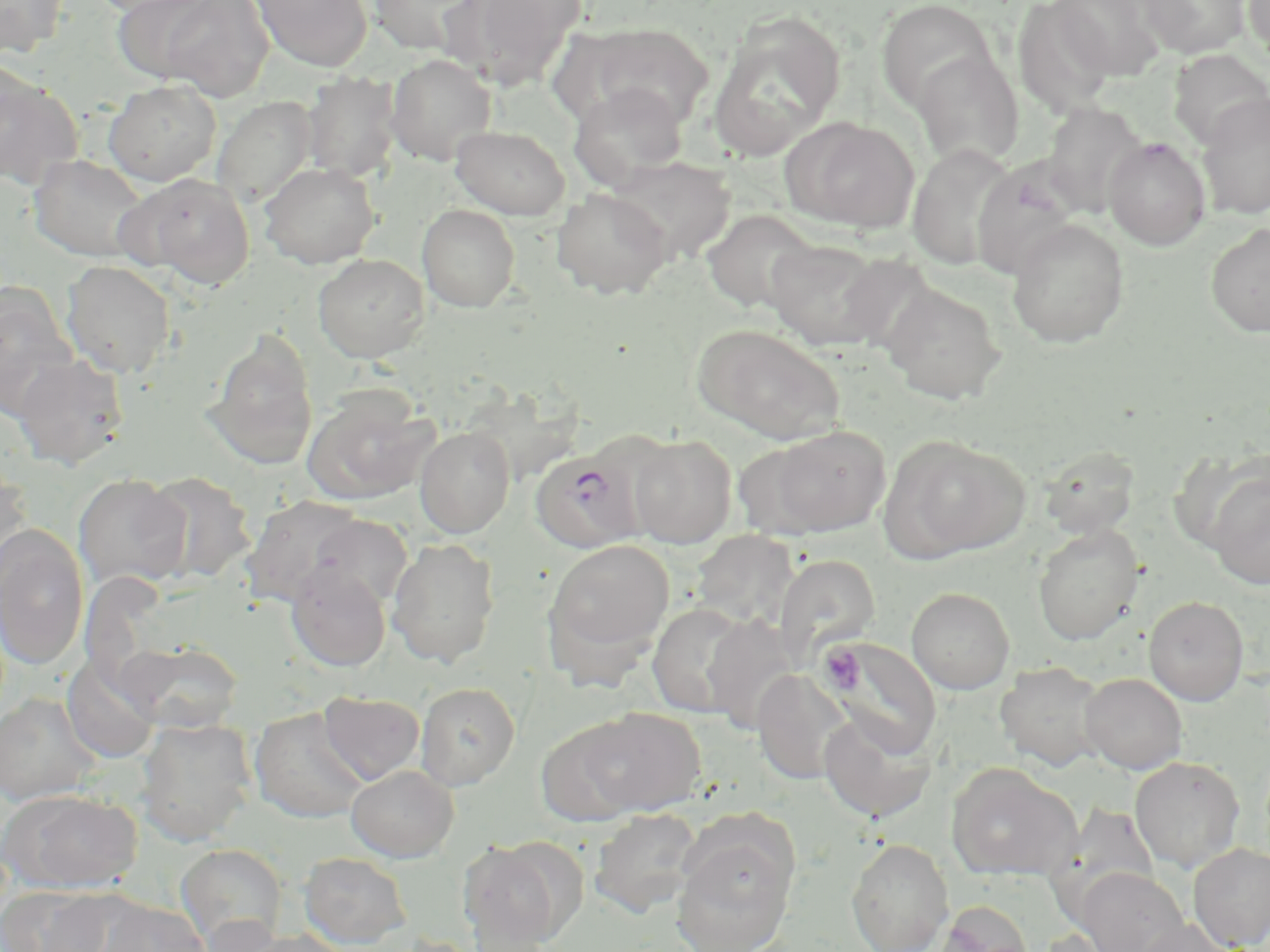
plasmodium_falciparum_infected_red_blood_cell_locations: 'approximate bounding boxes as [x1, y1, x2, y2] in pixels: [529, 445, 648, 553]'
slide_level_diagnosis: Plasmodium falciparum
preparation: thin blood film
uninfected_red_blood_cell_locations: 'approximate bounding boxes as [x1, y1, x2, y2] in pixels: [0, 0, 70, 57], [86, 0, 210, 17], [156, 0, 275, 101], [252, 0, 373, 72], [366, 0, 487, 56], [443, 0, 586, 89], [1049, 0, 1165, 81], [1138, 0, 1251, 59], [1243, 0, 1270, 66], [111, 1, 223, 84], [875, 1, 998, 115], [1012, 2, 1117, 118], [709, 16, 845, 158], [574, 23, 716, 129], [1168, 49, 1269, 150], [912, 51, 1024, 170], [385, 54, 497, 166], [302, 72, 401, 183], [0, 74, 83, 190], [103, 79, 222, 187], [569, 84, 688, 189], [1196, 92, 1270, 221], [212, 96, 318, 206], [1041, 101, 1148, 218], [780, 115, 920, 234], [450, 124, 570, 219], [1104, 137, 1210, 250], [907, 143, 1018, 271], [28, 153, 150, 263], [606, 156, 736, 265], [970, 158, 1082, 281], [258, 162, 379, 269], [119, 172, 256, 289], [552, 188, 672, 299], [417, 203, 520, 312], [701, 209, 821, 314], [1006, 219, 1129, 348], [1205, 223, 1270, 337], [763, 238, 895, 351], [313, 253, 430, 363], [60, 260, 176, 379], [879, 283, 1007, 405], [0, 288, 80, 419], [692, 324, 846, 445], [203, 329, 319, 470], [12, 354, 128, 470], [303, 387, 437, 505], [458, 388, 592, 485], [414, 424, 515, 538], [764, 425, 891, 537], [628, 434, 736, 548], [885, 436, 1030, 561], [1038, 445, 1140, 540], [0, 462, 32, 585], [1206, 469, 1270, 591], [144, 471, 256, 582], [72, 474, 192, 591], [241, 495, 369, 608], [304, 515, 413, 613], [0, 524, 89, 671], [1033, 524, 1144, 645], [690, 531, 800, 633], [386, 537, 500, 668], [542, 538, 675, 674], [774, 554, 880, 667], [286, 563, 391, 671], [906, 587, 1015, 694], [1144, 596, 1249, 705], [647, 601, 753, 718], [700, 613, 801, 734], [819, 636, 942, 758], [115, 640, 245, 734], [60, 655, 161, 765], [995, 661, 1108, 772], [751, 671, 849, 785], [1079, 673, 1187, 773], [415, 682, 520, 789], [318, 691, 425, 785], [0, 693, 101, 805], [576, 707, 705, 817], [249, 708, 369, 823], [817, 710, 938, 823], [136, 718, 256, 846], [1129, 756, 1245, 872], [946, 763, 1081, 883], [346, 765, 459, 862], [1, 789, 142, 895], [589, 807, 703, 918], [672, 833, 797, 952], [458, 837, 577, 950], [846, 838, 954, 952], [1188, 842, 1270, 950], [175, 843, 288, 949], [298, 852, 412, 948], [1077, 867, 1187, 952], [1, 885, 112, 952], [99, 899, 210, 952], [936, 901, 1033, 952], [1131, 918, 1242, 952], [231, 927, 358, 952]'
image_size: 1270×952 pixels
field_of_view: one of a larger specimen
platelet_locations: 'approximate bounding boxes as [x1, y1, x2, y2] in pixels: [819, 645, 862, 691]'
stain: May-Grünwald-Giemsa
magnification: 1000x
modality: optical microscopy